Locate every Plasmodium parasite.
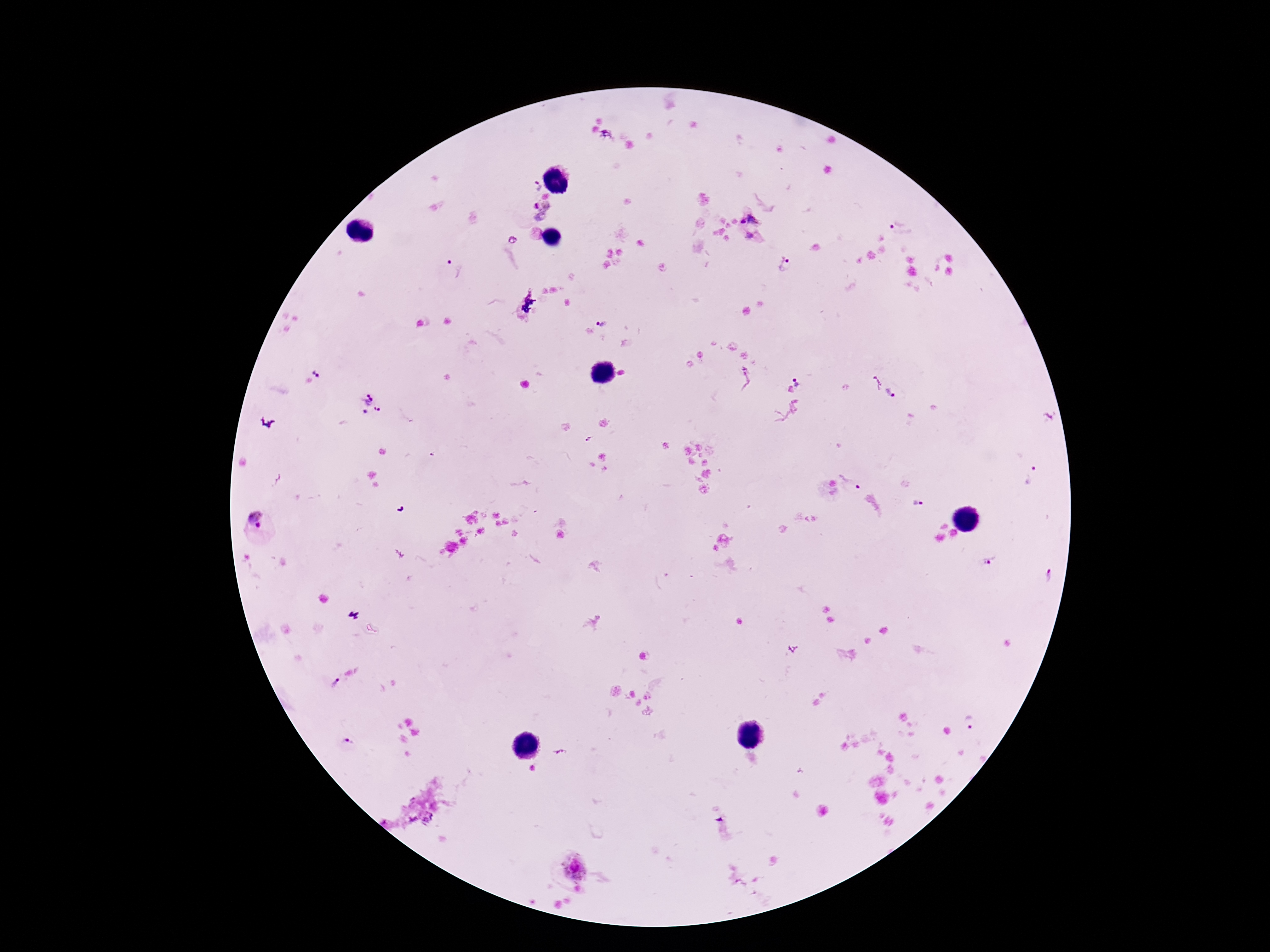

Approximate centers as (x, y) in pixels.
Plasmodium parasites: (608, 134), (536, 187), (541, 212), (752, 219), (901, 225), (536, 233), (752, 236), (512, 241), (787, 267), (453, 269), (602, 322), (320, 369), (745, 378), (798, 380), (876, 381), (891, 394), (368, 404), (588, 440), (1033, 477), (853, 482), (917, 502), (256, 518), (989, 562), (1048, 574), (334, 683), (970, 723), (350, 740), (561, 751), (573, 865).

Thick blood smear. Giemsa-stained preparation. Patient malaria status: infected. 100x magnification. Image is 1270×952 pixels. Smartphone photograph taken through the microscope eyepiece. One field from this slide.